Locate every blood parasite and identify its species.
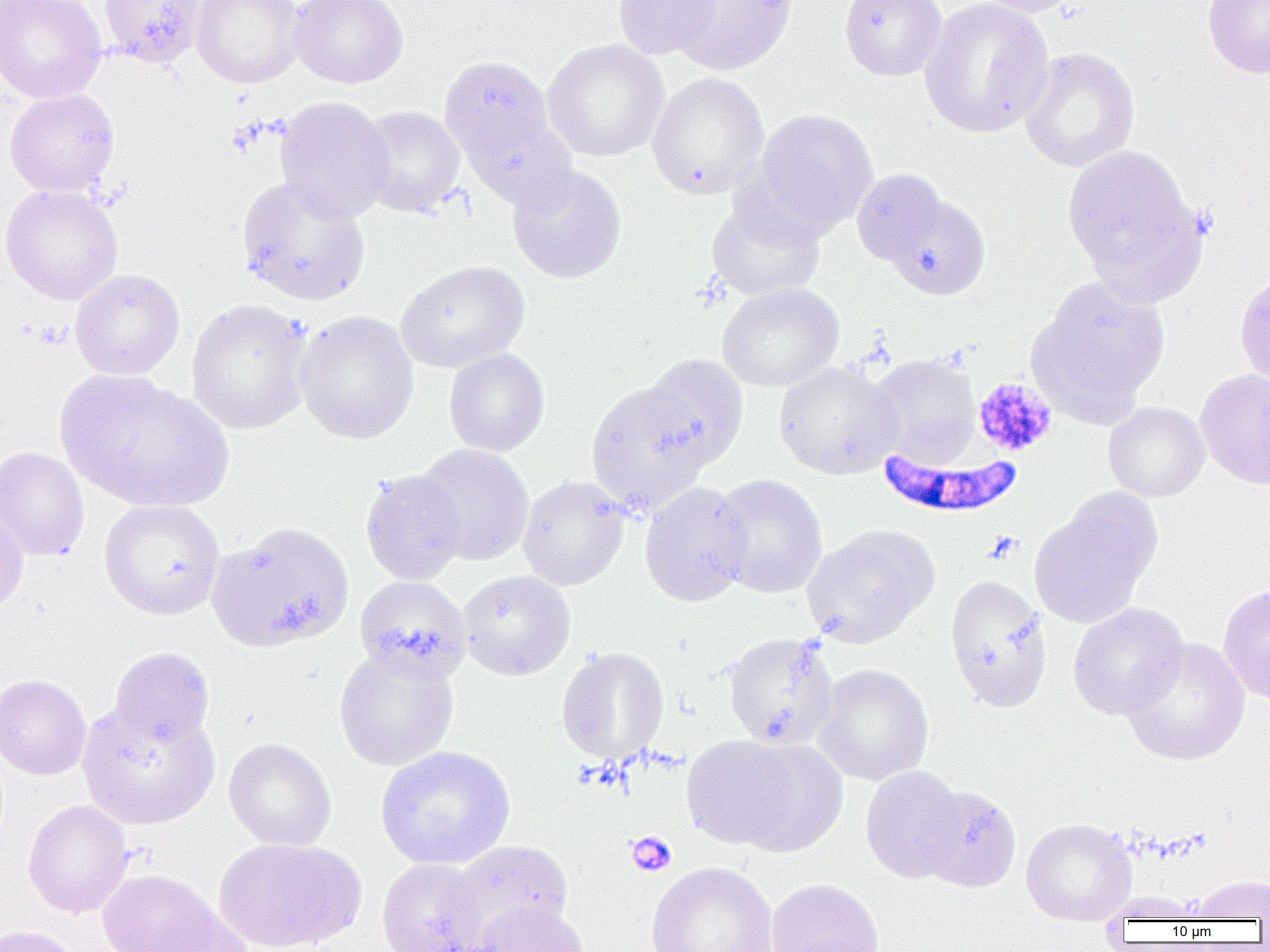
Approximate bounding boxes as [x1, y1, x2, y2] in pixels.
Plasmodium falciparum-infected red blood cells: [878, 448, 1022, 518].
No Plasmodium ovale, Plasmodium malariae, Plasmodium vivax, Babesia divergens, or Trypanosoma brucei observed.

Summary:
  - Platelet locations: [225, 120, 264, 158], [34, 321, 71, 350], [972, 377, 1057, 457], [985, 531, 1022, 563], [626, 831, 677, 877]
  - Uninfected red blood cell locations: [0, 0, 106, 102], [98, 0, 207, 68], [192, 0, 305, 88], [289, 0, 408, 88], [613, 0, 723, 60], [668, 0, 798, 75], [839, 0, 947, 81], [919, 0, 1054, 138], [970, 0, 1086, 17], [1202, 1, 1270, 79], [542, 39, 669, 162], [1019, 47, 1140, 173], [439, 53, 565, 189], [647, 72, 769, 199], [4, 89, 120, 197], [275, 96, 394, 222], [356, 105, 465, 218], [749, 108, 878, 236], [1062, 145, 1203, 296], [507, 164, 628, 284], [851, 168, 950, 268], [235, 176, 371, 307], [0, 184, 123, 305], [882, 192, 991, 300], [705, 199, 826, 303], [395, 260, 530, 373], [70, 268, 186, 380], [1235, 269, 1270, 390], [1027, 278, 1170, 420], [716, 283, 844, 393], [186, 298, 314, 435], [294, 311, 419, 445], [444, 348, 550, 457], [866, 353, 981, 464], [639, 354, 749, 470], [774, 361, 903, 479], [1195, 368, 1270, 491], [57, 369, 231, 511], [586, 381, 712, 513], [1103, 402, 1210, 502], [415, 444, 535, 565], [0, 446, 89, 561], [359, 469, 467, 585], [711, 474, 827, 598], [517, 475, 630, 590], [640, 481, 752, 607], [1029, 491, 1160, 629], [99, 499, 225, 620], [0, 504, 29, 616], [206, 521, 354, 654], [802, 526, 937, 648], [457, 570, 576, 680], [944, 574, 1052, 712], [354, 576, 470, 683], [1218, 584, 1270, 707], [1067, 603, 1189, 719], [722, 631, 840, 750], [1121, 637, 1250, 766], [333, 645, 459, 771], [109, 646, 215, 748], [556, 647, 669, 764], [813, 664, 934, 785], [0, 674, 91, 780], [77, 703, 220, 830], [682, 735, 804, 849], [224, 738, 336, 851], [733, 740, 846, 856], [375, 745, 516, 870], [861, 766, 967, 883], [917, 785, 1021, 892], [23, 800, 133, 918], [1021, 818, 1136, 925], [213, 837, 365, 951], [450, 840, 575, 943], [376, 858, 489, 952], [645, 861, 779, 952], [97, 868, 232, 951], [1190, 875, 1269, 921], [766, 878, 884, 952], [473, 901, 592, 952], [0, 924, 88, 952]
  - Slide-level diagnosis: Plasmodium falciparum
  - Preparation: thin blood film
  - Magnification: 1000x
  - Image size: 1270×952 pixels
  - Field of view: single
  - Modality: optical microscopy